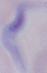
Summary:
  - Magnification: 1000x
  - Identification: trypanosome
  - Modality: photomicrograph